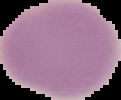
preparation = thin blood film
image size = 121×100 pixels
result = no malaria parasites detected
image type = segmented cell region with the area outside set to black